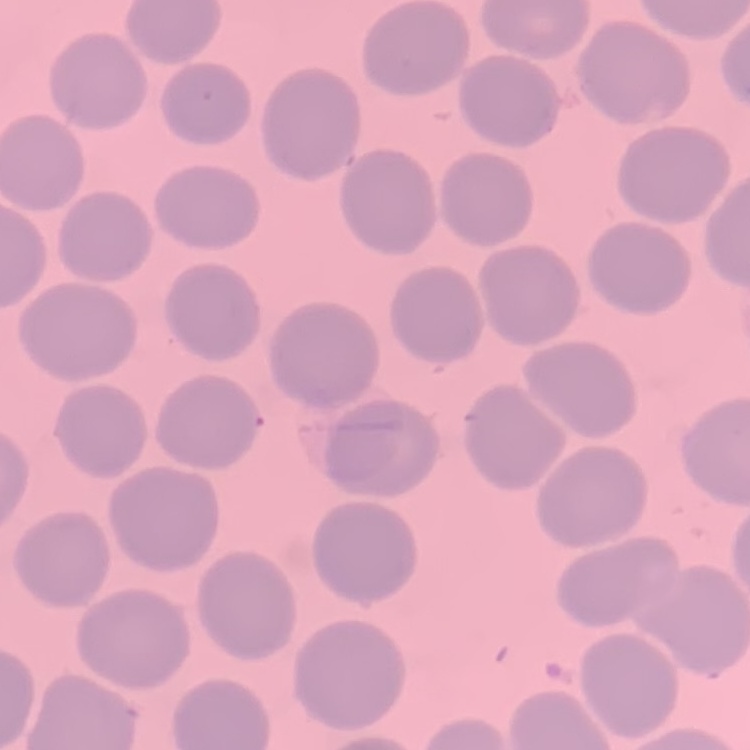
Summary:
  - Erythrocyte morphology: no rouleaux formation
  - Stain: Field's or Giemsa
  - Preparation: thin peripheral smear
  - Image type: one tile cut from a larger photomicrograph